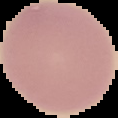 Image is 118×118 pixels. Cell region segmented out of the field of view; the surrounding area is masked to black. From a thin blood smear. Malaria status: uninfected.